Classify this cell by malaria status.
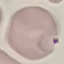
Parasitized.

Photographed with a smartphone camera at the microscope eyepiece. Automatically extracted cell patch, resized to 64 × 64 pixels. Thin blood smear. Giemsa stain.